Classify this cell by malaria status.
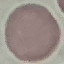

It is uninfected.

Summary:
  - Capture: smartphone through the microscope eyepiece
  - Image type: cell patch, automatically extracted from a larger field of view and resized to 64 × 64 pixels
  - Preparation: thin smear
  - Stain: Giemsa